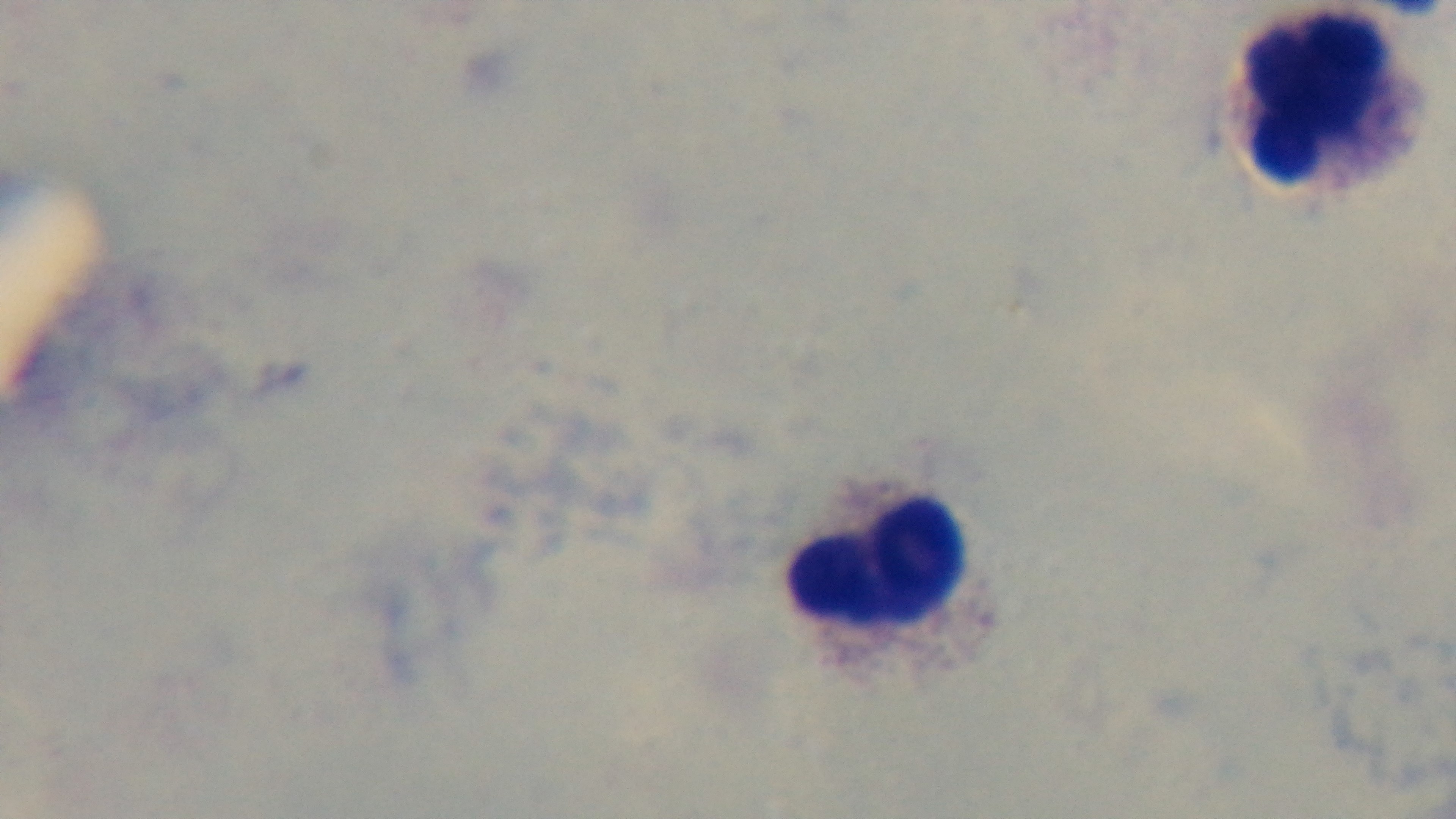 Single field of view. 100x oil-immersion objective. Light microscopy. Giemsa-stained. Mounted 4K digital camera. Malaria status: negative. Preparation: thick smear.